Locate every blood parasite and identify its species.
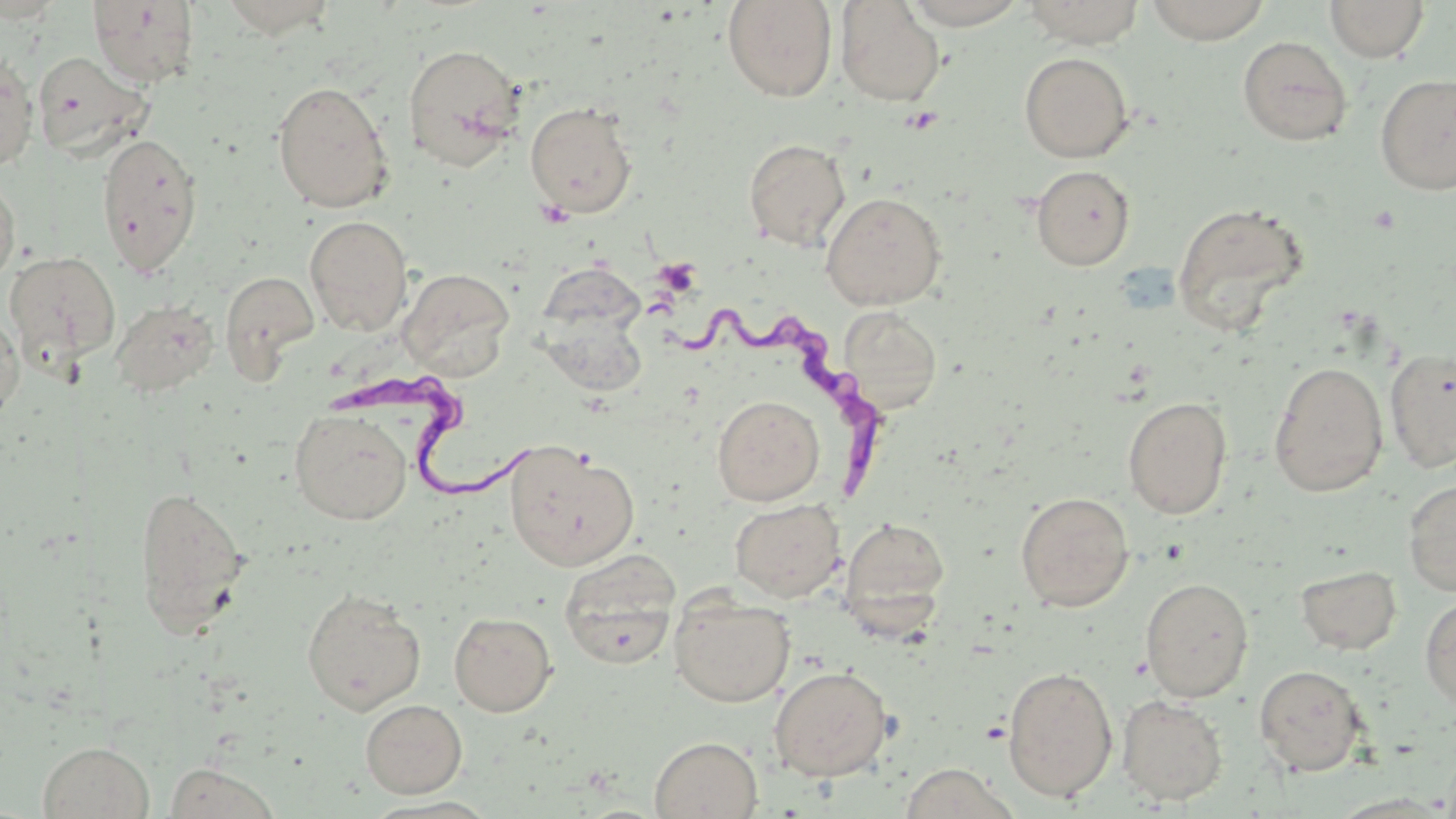
Approximate bounding boxes as (x1, y1, x2, y2) in pixels.
Trypanosoma brucei: (666, 295, 885, 502), (335, 366, 551, 507).
No Plasmodium falciparum, Plasmodium ovale, Plasmodium malariae, Plasmodium vivax, or Babesia divergens observed.

Platelet locations: (655, 258, 701, 296). Uninfected red blood cell locations: (0, 0, 67, 23), (722, 0, 838, 102), (901, 0, 1030, 28), (1022, 0, 1147, 48), (1145, 0, 1272, 44), (1325, 0, 1429, 62), (88, 1, 199, 87), (835, 1, 946, 106), (1237, 36, 1353, 146), (402, 42, 526, 172), (31, 51, 154, 161), (1019, 52, 1134, 162), (0, 53, 39, 170), (1375, 73, 1456, 195), (271, 80, 395, 213), (524, 101, 638, 218), (96, 132, 204, 276), (743, 138, 851, 251), (1031, 165, 1135, 270), (0, 172, 20, 288), (821, 191, 947, 310), (1170, 201, 1311, 334), (305, 216, 413, 337), (3, 250, 121, 373), (536, 262, 646, 344), (398, 268, 515, 380), (221, 269, 318, 376), (110, 298, 219, 397), (836, 306, 943, 414), (0, 307, 24, 422), (539, 310, 649, 398), (1384, 347, 1456, 473), (1268, 362, 1388, 497), (713, 395, 824, 506), (1122, 396, 1233, 519), (290, 409, 412, 525), (503, 442, 640, 573), (1403, 477, 1456, 596), (133, 485, 251, 633), (1015, 491, 1134, 612), (729, 498, 844, 602), (839, 516, 951, 631), (559, 553, 680, 669), (1295, 564, 1402, 655), (1140, 577, 1254, 702), (302, 588, 426, 714), (1420, 593, 1456, 711), (670, 595, 795, 707), (448, 611, 557, 716), (1254, 664, 1369, 776), (768, 665, 893, 781), (1002, 665, 1118, 802), (1116, 694, 1228, 805), (360, 698, 468, 798), (649, 735, 763, 818), (37, 741, 154, 819), (163, 761, 284, 819). Slide-level diagnosis: Trypanosoma brucei. Captured at 1000x magnification. May-Grünwald-Giemsa stain. Image is 1456×819 pixels. Thin blood smear. Single field of view. Optical microscopy.